Locate every Plasmodium ovale-infected red blood cell.
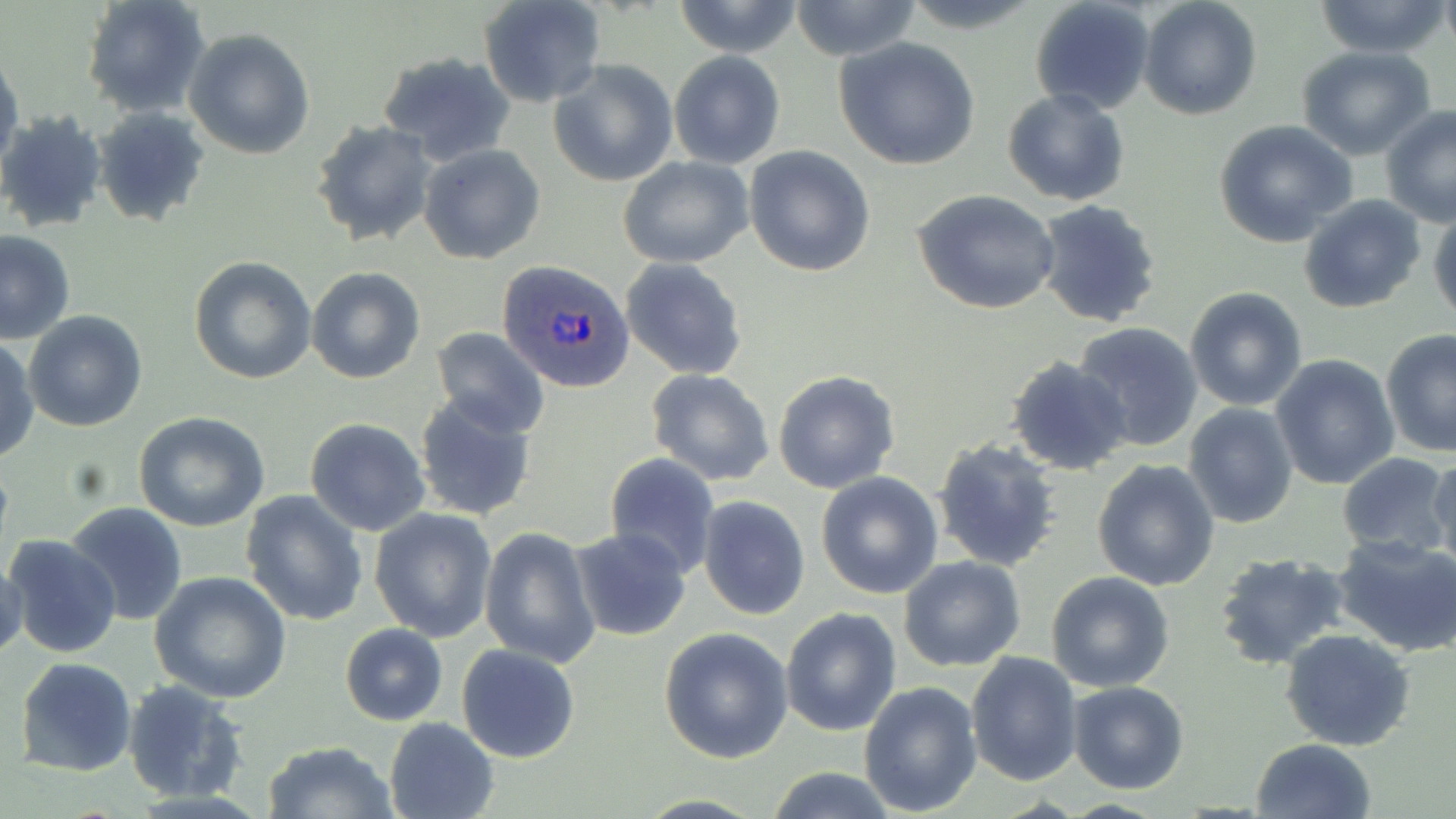

Approximate bounding boxes as (x1, y1, x2, y2) in pixels.
Plasmodium ovale-infected red blood cells: (497, 259, 635, 394).

Uninfected red blood cell locations: (81, 0, 211, 117), (672, 0, 806, 57), (898, 0, 1044, 32), (1029, 0, 1157, 115), (1138, 0, 1262, 121), (478, 1, 607, 107), (789, 1, 921, 58), (1312, 1, 1451, 57), (183, 28, 315, 158), (833, 38, 981, 170), (1296, 47, 1436, 159), (396, 48, 530, 266), (0, 49, 24, 178), (668, 50, 786, 169), (377, 51, 515, 167), (1250, 53, 1396, 201), (548, 60, 678, 187), (1002, 88, 1129, 206), (1380, 105, 1456, 228), (91, 109, 212, 227), (0, 110, 107, 232), (311, 120, 437, 247), (1214, 120, 1357, 248), (419, 144, 546, 265), (744, 147, 875, 279), (617, 156, 754, 268), (913, 190, 1062, 316), (1299, 194, 1427, 314), (1033, 198, 1165, 329), (1428, 209, 1456, 334), (0, 229, 75, 343), (188, 257, 317, 384), (620, 259, 747, 382), (307, 267, 425, 384), (1184, 287, 1307, 410), (23, 311, 148, 431), (1074, 321, 1205, 452), (429, 327, 550, 437), (1380, 330, 1456, 457), (0, 336, 38, 464), (1271, 355, 1399, 490), (1007, 356, 1134, 477), (646, 368, 775, 487), (773, 370, 900, 494), (412, 391, 537, 523), (1184, 403, 1298, 530), (136, 413, 270, 532), (305, 418, 431, 537), (933, 438, 1064, 573), (604, 452, 720, 578), (1336, 453, 1453, 556), (1427, 456, 1455, 572), (1092, 459, 1222, 592), (816, 472, 943, 598), (240, 488, 370, 629), (698, 494, 811, 622), (62, 502, 187, 624), (369, 507, 497, 642), (480, 527, 599, 667), (568, 527, 692, 643), (4, 534, 120, 660), (1331, 535, 1456, 658), (1211, 552, 1354, 674), (0, 557, 27, 664), (899, 557, 1026, 672), (1045, 570, 1174, 693), (150, 572, 293, 703), (780, 608, 902, 736), (340, 623, 448, 726), (659, 626, 794, 763), (1282, 629, 1415, 751), (456, 643, 582, 765), (966, 651, 1082, 786), (14, 656, 139, 777), (121, 679, 250, 803), (1067, 681, 1189, 793), (859, 682, 981, 815), (384, 716, 500, 819), (1252, 738, 1377, 819), (262, 740, 399, 819), (761, 767, 901, 819), (631, 794, 770, 819). Slide-level diagnosis: Plasmodium ovale. Thin blood film. Optical microscopy. 1000x magnification. One field of a larger specimen. Image is 1456×819 pixels. May-Grünwald-Giemsa-stained preparation.